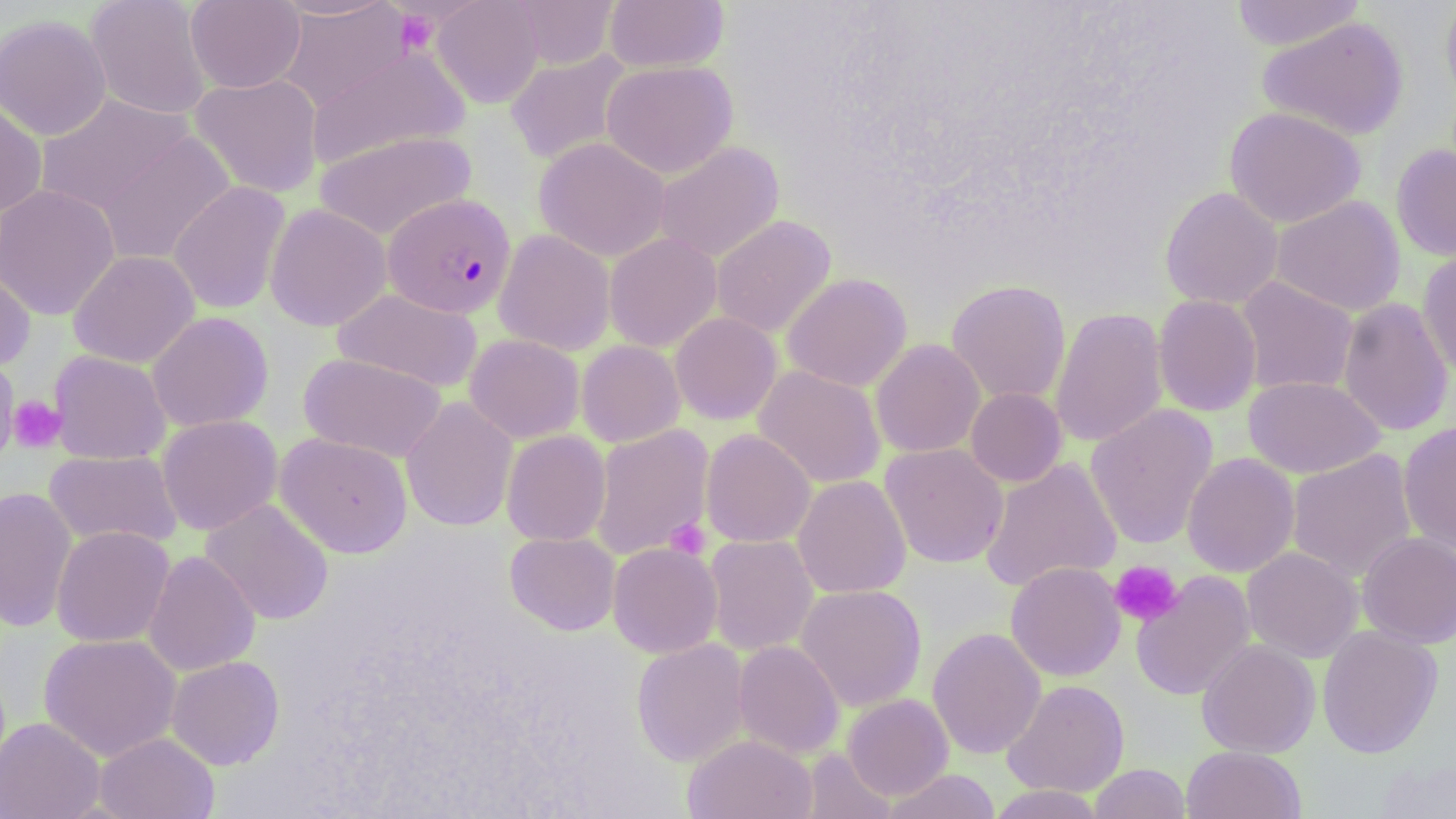
{
  "slide_level_diagnosis": "Plasmodium falciparum",
  "stain": "May-Grünwald-Giemsa",
  "modality": "light microscopy",
  "image_size": "1456×819 pixels",
  "platelet_locations": "approximate bounding boxes as named x1/y1/x2/y2 corners in pixels: (x1=394, y1=8, x2=439, y2=55), (x1=7, y1=395, x2=66, y2=453), (x1=665, y1=518, x2=711, y2=560), (x1=1109, y1=560, x2=1183, y2=627)",
  "field_of_view": "single",
  "preparation": "thin blood film",
  "plasmodium_falciparum_infected_red_blood_cell_locations": "approximate bounding boxes as named x1/y1/x2/y2 corners in pixels: (x1=383, y1=193, x2=516, y2=319)",
  "uninfected_red_blood_cell_locations": "approximate bounding boxes as named x1/y1/x2/y2 corners in pixels: (x1=85, y1=0, x2=212, y2=120), (x1=186, y1=0, x2=305, y2=93), (x1=271, y1=0, x2=400, y2=19), (x1=431, y1=0, x2=544, y2=108), (x1=509, y1=0, x2=619, y2=69), (x1=604, y1=0, x2=729, y2=73), (x1=1230, y1=0, x2=1366, y2=51), (x1=1440, y1=0, x2=1456, y2=110), (x1=277, y1=2, x2=413, y2=112), (x1=0, y1=14, x2=112, y2=141), (x1=1257, y1=17, x2=1409, y2=141), (x1=307, y1=47, x2=470, y2=169), (x1=504, y1=51, x2=633, y2=165), (x1=601, y1=60, x2=738, y2=178), (x1=190, y1=73, x2=323, y2=198), (x1=35, y1=94, x2=194, y2=216), (x1=0, y1=99, x2=48, y2=216), (x1=1224, y1=105, x2=1366, y2=228), (x1=314, y1=130, x2=476, y2=240), (x1=94, y1=131, x2=235, y2=266), (x1=534, y1=137, x2=671, y2=262), (x1=654, y1=142, x2=784, y2=262), (x1=1391, y1=143, x2=1456, y2=262), (x1=168, y1=181, x2=291, y2=315), (x1=0, y1=184, x2=121, y2=321), (x1=1159, y1=186, x2=1284, y2=309), (x1=1271, y1=196, x2=1406, y2=316), (x1=265, y1=203, x2=392, y2=332), (x1=711, y1=215, x2=836, y2=338), (x1=494, y1=229, x2=615, y2=356), (x1=604, y1=233, x2=722, y2=353), (x1=68, y1=250, x2=200, y2=368), (x1=1417, y1=250, x2=1456, y2=380), (x1=0, y1=261, x2=36, y2=371), (x1=782, y1=272, x2=912, y2=392), (x1=1235, y1=277, x2=1358, y2=396), (x1=946, y1=279, x2=1071, y2=405), (x1=332, y1=288, x2=484, y2=393), (x1=1152, y1=294, x2=1262, y2=417), (x1=1337, y1=298, x2=1454, y2=436), (x1=1049, y1=306, x2=1168, y2=448), (x1=147, y1=311, x2=273, y2=432), (x1=670, y1=312, x2=782, y2=425), (x1=465, y1=334, x2=585, y2=443), (x1=870, y1=339, x2=985, y2=458), (x1=576, y1=340, x2=685, y2=447), (x1=48, y1=350, x2=171, y2=465), (x1=299, y1=352, x2=447, y2=463), (x1=1, y1=355, x2=21, y2=466), (x1=753, y1=365, x2=886, y2=489), (x1=1243, y1=376, x2=1384, y2=478), (x1=966, y1=387, x2=1067, y2=487), (x1=400, y1=397, x2=518, y2=533), (x1=1085, y1=405, x2=1218, y2=549), (x1=156, y1=415, x2=282, y2=535), (x1=1398, y1=422, x2=1456, y2=552), (x1=590, y1=424, x2=714, y2=560), (x1=701, y1=429, x2=815, y2=548), (x1=502, y1=430, x2=611, y2=546), (x1=275, y1=432, x2=413, y2=558), (x1=880, y1=443, x2=1009, y2=569), (x1=1286, y1=449, x2=1417, y2=582), (x1=43, y1=450, x2=181, y2=549), (x1=1182, y1=452, x2=1300, y2=577), (x1=979, y1=457, x2=1122, y2=592), (x1=792, y1=475, x2=911, y2=599), (x1=0, y1=486, x2=77, y2=632), (x1=200, y1=498, x2=334, y2=625), (x1=51, y1=526, x2=175, y2=647), (x1=505, y1=532, x2=620, y2=635), (x1=1357, y1=532, x2=1456, y2=648), (x1=703, y1=534, x2=818, y2=656), (x1=608, y1=542, x2=723, y2=659), (x1=1242, y1=547, x2=1363, y2=662), (x1=144, y1=550, x2=260, y2=676), (x1=1005, y1=561, x2=1125, y2=681), (x1=1132, y1=571, x2=1256, y2=700), (x1=795, y1=584, x2=927, y2=711), (x1=1317, y1=625, x2=1443, y2=758), (x1=927, y1=627, x2=1047, y2=759), (x1=38, y1=633, x2=182, y2=762), (x1=631, y1=639, x2=750, y2=767), (x1=733, y1=640, x2=845, y2=759), (x1=1197, y1=640, x2=1320, y2=758), (x1=166, y1=655, x2=285, y2=770), (x1=1002, y1=678, x2=1129, y2=797), (x1=843, y1=694, x2=953, y2=800), (x1=0, y1=717, x2=104, y2=819), (x1=95, y1=732, x2=219, y2=819), (x1=682, y1=734, x2=817, y2=819), (x1=1181, y1=745, x2=1307, y2=819), (x1=801, y1=749, x2=897, y2=818), (x1=1375, y1=758, x2=1456, y2=818), (x1=1089, y1=763, x2=1190, y2=819), (x1=882, y1=769, x2=1002, y2=819), (x1=984, y1=785, x2=1111, y2=818)",
  "magnification": "1000x"
}